Point out every Plasmodium parasite and every leukocyte.
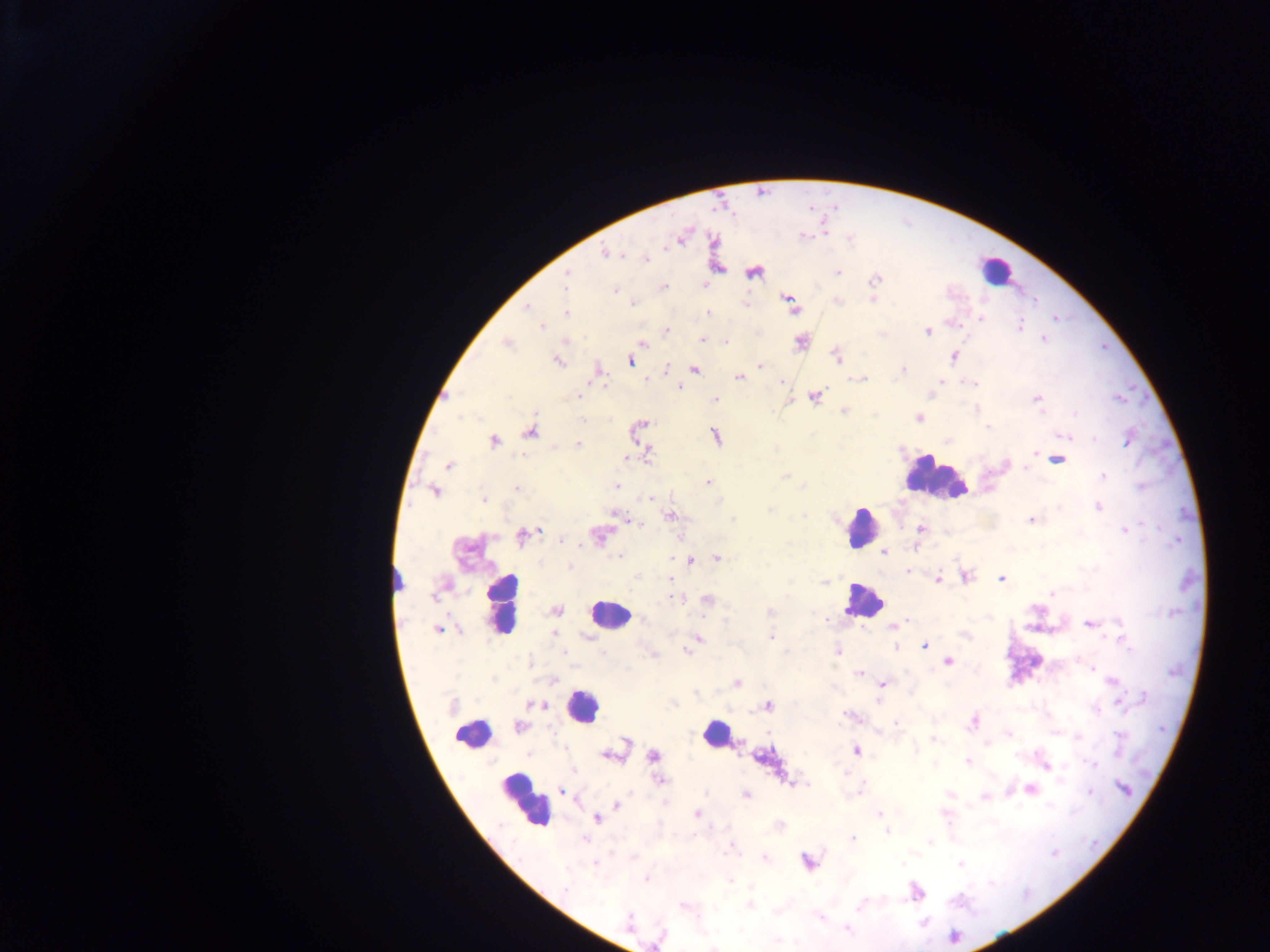

Approximate centers as {x, y} in pixels.
Plasmodium parasites: {805, 236}, {849, 240}, {607, 253}, {645, 259}, {753, 272}, {837, 272}, {567, 277}, {875, 279}, {703, 285}, {664, 287}, {614, 289}, {790, 302}, {838, 302}, {633, 304}, {526, 308}, {565, 313}, {709, 313}, {981, 318}, {542, 326}, {1020, 326}, {666, 330}, {927, 331}, {701, 339}, {1043, 339}, {642, 341}, {725, 342}, {800, 342}, {508, 343}, {954, 356}, {837, 357}, {630, 360}, {559, 361}, {760, 366}, {695, 370}, {903, 370}, {599, 374}, {739, 377}, {861, 379}, {942, 381}, {781, 382}, {971, 382}, {679, 387}, {578, 395}, {814, 397}, {1117, 398}, {715, 399}, {1037, 399}, {843, 411}, {1075, 414}, {918, 417}, {581, 420}, {641, 425}, {989, 428}, {530, 431}, {715, 436}, {1065, 437}, {1093, 439}, {1128, 440}, {494, 441}, {577, 445}, {648, 454}, {1035, 454}, {628, 457}, {1058, 459}, {448, 466}, {1103, 475}, {785, 476}, {708, 482}, {616, 485}, {516, 489}, {434, 491}, {649, 498}, {484, 500}, {1098, 507}, {770, 509}, {617, 515}, {671, 516}, {1031, 521}, {637, 523}, {920, 529}, {1125, 531}, {598, 534}, {524, 535}, {562, 539}, {917, 548}, {885, 552}, {618, 556}, {717, 558}, {690, 560}, {570, 567}, {908, 572}, {967, 577}, {939, 579}, {1001, 579}, {670, 580}, {1051, 593}, {676, 599}, {708, 600}, {556, 610}, {770, 612}, {827, 619}, {908, 619}, {1119, 623}, {1090, 624}, {899, 625}, {892, 627}, {438, 630}, {771, 637}, {1121, 639}, {697, 640}, {925, 645}, {895, 647}, {687, 650}, {837, 651}, {948, 661}, {1092, 667}, {859, 674}, {1112, 681}, {737, 683}, {883, 684}, {1144, 697}, {878, 701}, {1119, 703}, {537, 705}, {768, 705}, {847, 715}, {973, 722}, {895, 723}, {520, 726}, {1009, 733}, {933, 740}, {626, 742}, {857, 751}, {609, 756}, {654, 756}, {968, 762}, {1094, 764}, {1045, 765}, {574, 770}, {660, 780}, {1124, 788}, {862, 789}, {1031, 789}, {563, 792}, {1090, 793}, {746, 795}, {617, 804}, {697, 814}, {879, 814}, {597, 818}, {888, 831}, {584, 840}, {852, 840}, {930, 841}, {1054, 853}, {765, 857}, {807, 862}, {903, 863}, {960, 863}, {595, 864}, {646, 879}, {731, 880}, {565, 888}, {916, 893}, {750, 905}, {683, 906}, {859, 906}, {820, 918}, {628, 920}, {848, 930}, {953, 937}, {713, 947}.
Leukocytes: {995, 270}, {935, 479}, {862, 526}, {862, 600}, {501, 604}, {609, 614}, {583, 707}, {715, 733}, {472, 736}, {524, 801}.

preparation: thick blood film
image_size: 1270×952 pixels
capture: mobile-phone photograph through a microscope
field_of_view: single
country: Ghana